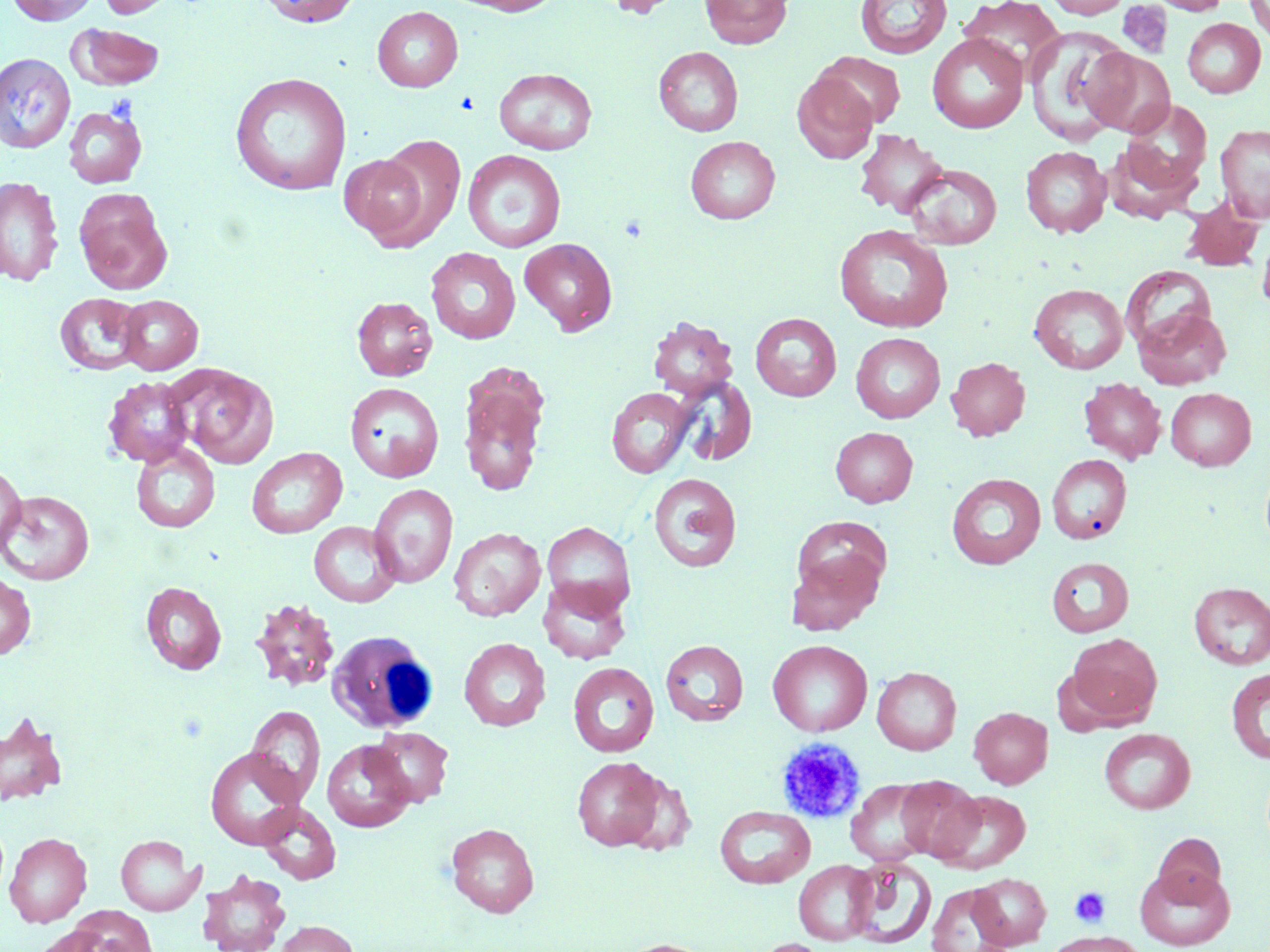 Approximate bounding boxes as named x1/y1/x2/y2 corners in pixels. White blood cell locations: (x1=326, y1=630, x2=439, y2=734). Uninfected red blood cell locations (subset): (x1=6, y1=0, x2=99, y2=25), (x1=98, y1=0, x2=178, y2=18), (x1=257, y1=0, x2=360, y2=27), (x1=447, y1=0, x2=565, y2=16), (x1=600, y1=0, x2=686, y2=18), (x1=700, y1=0, x2=792, y2=49), (x1=856, y1=0, x2=952, y2=59), (x1=959, y1=0, x2=1065, y2=79), (x1=1044, y1=0, x2=1131, y2=18), (x1=1149, y1=0, x2=1230, y2=15), (x1=1245, y1=0, x2=1270, y2=46), (x1=372, y1=6, x2=463, y2=92), (x1=1182, y1=18, x2=1265, y2=98), (x1=67, y1=22, x2=165, y2=90), (x1=1025, y1=26, x2=1132, y2=145), (x1=927, y1=33, x2=1027, y2=133), (x1=653, y1=47, x2=743, y2=136), (x1=1082, y1=47, x2=1174, y2=137), (x1=816, y1=52, x2=906, y2=127), (x1=0, y1=53, x2=75, y2=152), (x1=494, y1=68, x2=598, y2=154), (x1=229, y1=72, x2=352, y2=196), (x1=792, y1=72, x2=878, y2=164), (x1=1117, y1=99, x2=1213, y2=200), (x1=63, y1=106, x2=147, y2=188), (x1=1215, y1=123, x2=1270, y2=223), (x1=854, y1=129, x2=949, y2=219), (x1=367, y1=134, x2=467, y2=249), (x1=685, y1=136, x2=780, y2=224), (x1=1020, y1=146, x2=1112, y2=238), (x1=463, y1=149, x2=566, y2=252), (x1=338, y1=150, x2=434, y2=246), (x1=904, y1=163, x2=1002, y2=249), (x1=0, y1=176, x2=64, y2=287), (x1=74, y1=189, x2=172, y2=294), (x1=1179, y1=195, x2=1267, y2=273), (x1=834, y1=224, x2=953, y2=333), (x1=1257, y1=225, x2=1270, y2=318), (x1=520, y1=238, x2=617, y2=335), (x1=426, y1=247, x2=520, y2=344), (x1=1120, y1=265, x2=1216, y2=352), (x1=1029, y1=283, x2=1128, y2=373), (x1=54, y1=293, x2=148, y2=375), (x1=117, y1=295, x2=203, y2=374), (x1=352, y1=296, x2=437, y2=381), (x1=1134, y1=307, x2=1231, y2=389), (x1=750, y1=312, x2=841, y2=401), (x1=648, y1=316, x2=738, y2=399), (x1=851, y1=332, x2=945, y2=422), (x1=946, y1=356, x2=1030, y2=440), (x1=458, y1=362, x2=550, y2=498), (x1=173, y1=364, x2=278, y2=467), (x1=102, y1=376, x2=196, y2=467), (x1=672, y1=377, x2=758, y2=466), (x1=1079, y1=377, x2=1167, y2=464), (x1=345, y1=382, x2=444, y2=482), (x1=606, y1=387, x2=695, y2=478), (x1=1165, y1=387, x2=1256, y2=470), (x1=830, y1=427, x2=918, y2=507), (x1=130, y1=442, x2=221, y2=533), (x1=246, y1=447, x2=347, y2=538), (x1=1046, y1=453, x2=1132, y2=544), (x1=0, y1=463, x2=26, y2=556), (x1=648, y1=473, x2=742, y2=572), (x1=946, y1=473, x2=1046, y2=569), (x1=369, y1=484, x2=458, y2=588), (x1=1, y1=490, x2=94, y2=585), (x1=791, y1=516, x2=893, y2=602), (x1=309, y1=521, x2=402, y2=607), (x1=541, y1=521, x2=636, y2=615), (x1=448, y1=527, x2=546, y2=621), (x1=786, y1=551, x2=883, y2=634), (x1=1046, y1=556, x2=1134, y2=637), (x1=0, y1=572, x2=36, y2=660), (x1=537, y1=578, x2=632, y2=665), (x1=140, y1=581, x2=227, y2=675), (x1=1189, y1=582, x2=1270, y2=669), (x1=249, y1=596, x2=341, y2=693), (x1=1066, y1=632, x2=1162, y2=726), (x1=459, y1=638, x2=551, y2=731), (x1=768, y1=639, x2=872, y2=736), (x1=660, y1=640, x2=749, y2=725), (x1=568, y1=662, x2=659, y2=757), (x1=872, y1=667, x2=961, y2=754), (x1=1226, y1=667, x2=1270, y2=764), (x1=246, y1=705, x2=325, y2=804), (x1=969, y1=707, x2=1052, y2=788), (x1=0, y1=711, x2=68, y2=806), (x1=368, y1=726, x2=454, y2=807), (x1=1099, y1=728, x2=1195, y2=814), (x1=321, y1=739, x2=415, y2=832), (x1=205, y1=747, x2=306, y2=849), (x1=572, y1=756, x2=665, y2=851), (x1=620, y1=773, x2=697, y2=856), (x1=895, y1=776, x2=984, y2=862), (x1=846, y1=779, x2=935, y2=866), (x1=934, y1=790, x2=1031, y2=873), (x1=259, y1=802, x2=341, y2=884), (x1=714, y1=806, x2=815, y2=888), (x1=446, y1=823, x2=539, y2=918), (x1=4, y1=832, x2=91, y2=927), (x1=1150, y1=832, x2=1226, y2=903), (x1=116, y1=835, x2=202, y2=916), (x1=846, y1=856, x2=936, y2=948), (x1=793, y1=860, x2=878, y2=945), (x1=1135, y1=864, x2=1235, y2=950), (x1=196, y1=870, x2=291, y2=952), (x1=970, y1=873, x2=1051, y2=949), (x1=926, y1=883, x2=1013, y2=952), (x1=66, y1=906, x2=158, y2=952), (x1=274, y1=919, x2=358, y2=952), (x1=32, y1=926, x2=111, y2=952), (x1=1044, y1=930, x2=1146, y2=952), (x1=615, y1=938, x2=718, y2=952), (x1=752, y1=938, x2=837, y2=952). Platelet locations (subset): (x1=455, y1=92, x2=478, y2=115), (x1=105, y1=94, x2=138, y2=123), (x1=775, y1=737, x2=866, y2=823), (x1=1069, y1=886, x2=1111, y2=927). Slide-level diagnosis: no evidence of blood parasites. Single field of view. Captured at 1000x magnification. Thin blood smear. Light microscopy. Image is 1270×952 pixels. May-Grünwald-Giemsa-stained preparation.